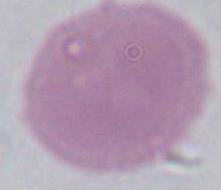
{
  "identification": "red blood cell",
  "magnification": "1000x",
  "modality": "micrograph"
}